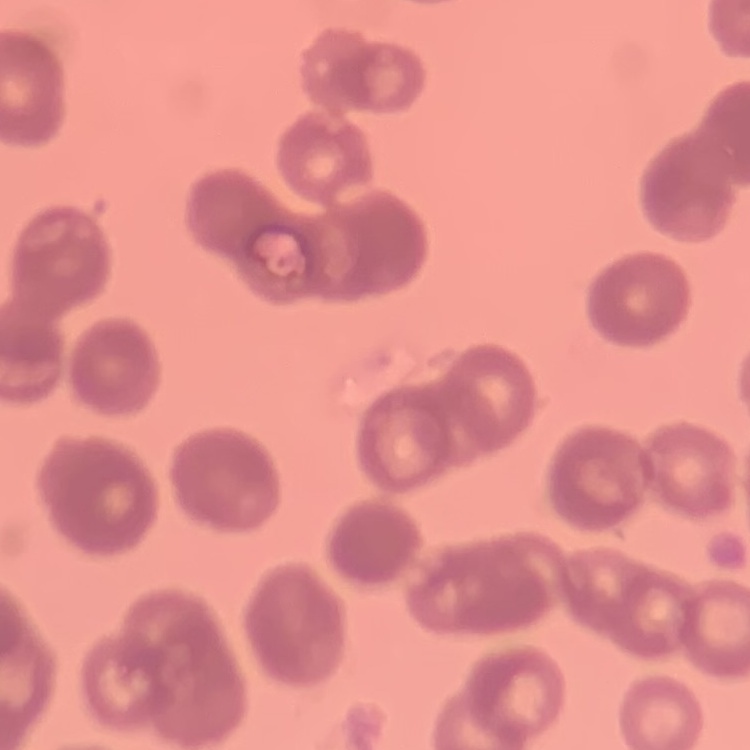
Summary:
  - Erythrocyte morphology: rouleaux formation
  - Image type: square crop of a larger photomicrograph
  - Preparation: thin blood film
  - Stain: Field's or Giemsa